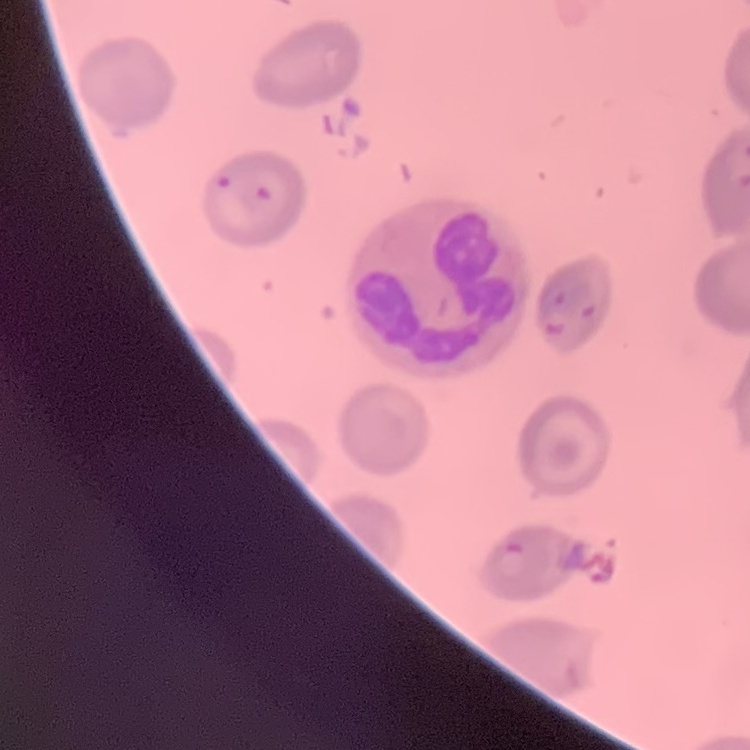

erythrocyte_morphology: no rouleaux formation
stain: Field's or Giemsa
image_type: square crop of a larger photomicrograph
preparation: thin peripheral smear